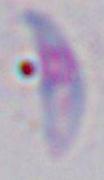

{
  "modality": "photomicrograph",
  "magnification": "1000x",
  "identification": "Toxoplasma gondii"
}